State the blood parasite species.
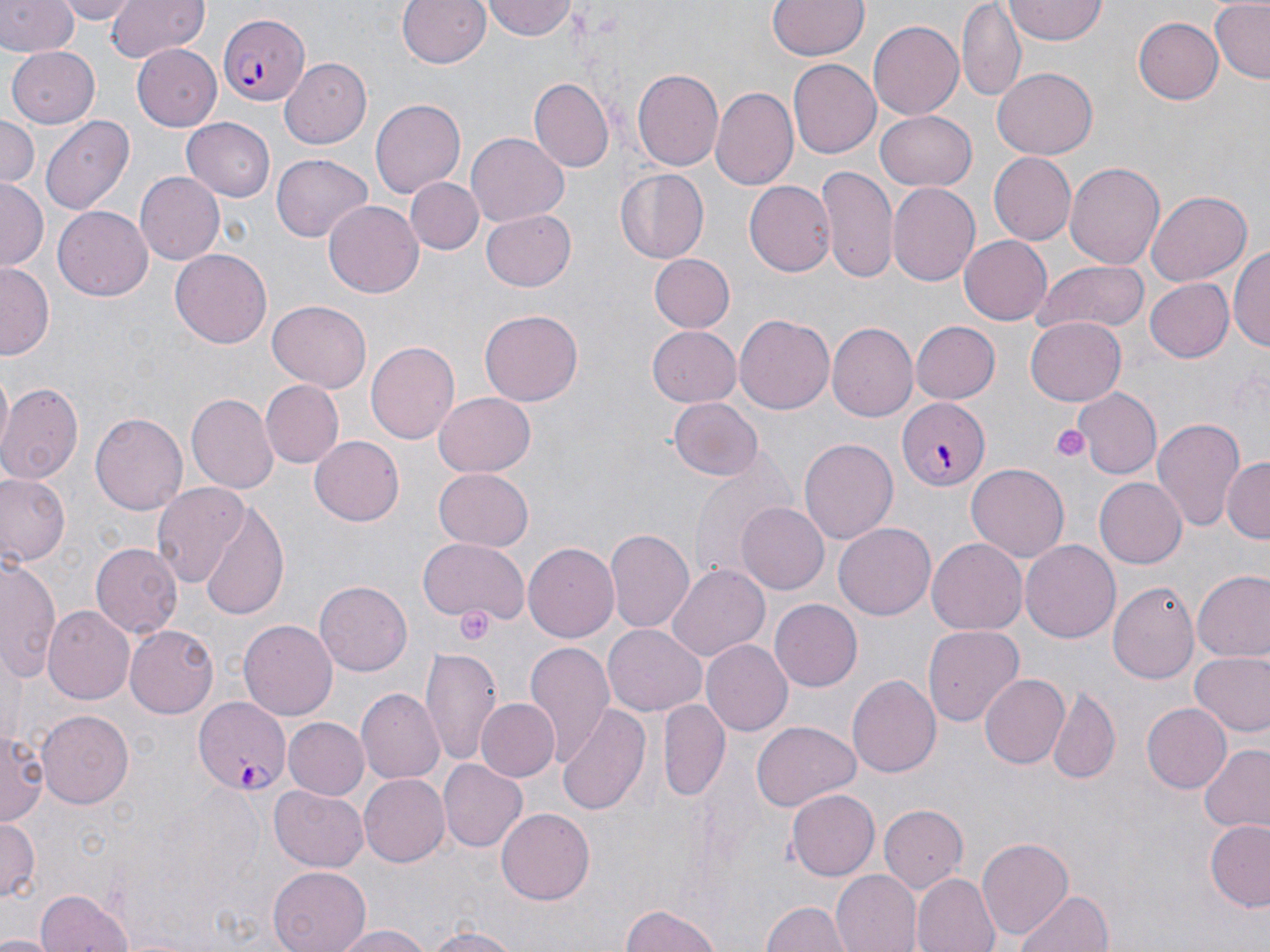
Plasmodium falciparum.

uninfected red blood cell locations = approximate bounding boxes as [x1, y1, x2, y2] in pixels: [0, 0, 76, 57], [56, 0, 140, 24], [103, 0, 209, 65], [396, 0, 492, 70], [481, 0, 578, 41], [767, 0, 868, 60], [1210, 0, 1269, 84], [957, 3, 1026, 101], [1005, 3, 1111, 44], [1134, 17, 1223, 105], [868, 21, 964, 121], [136, 44, 222, 133], [6, 47, 100, 127], [280, 58, 371, 148], [787, 59, 881, 158], [994, 69, 1097, 157], [632, 70, 722, 172], [531, 78, 614, 170], [710, 86, 798, 192], [371, 98, 464, 200], [876, 109, 977, 190], [0, 114, 38, 191], [182, 116, 276, 200], [42, 117, 135, 215], [467, 134, 568, 227], [991, 151, 1078, 245], [272, 155, 372, 244], [1065, 161, 1164, 270], [818, 166, 897, 282], [614, 169, 710, 264], [135, 172, 225, 266], [407, 178, 483, 253], [0, 179, 47, 268], [743, 180, 836, 276], [887, 182, 979, 287], [1147, 188, 1252, 284], [324, 200, 422, 298], [53, 204, 153, 297], [483, 209, 576, 291], [959, 234, 1052, 325], [1232, 242, 1270, 356], [170, 248, 273, 348], [647, 253, 735, 332], [1031, 261, 1150, 336], [0, 264, 52, 359], [1144, 278, 1234, 364], [266, 301, 371, 394], [480, 310, 582, 406], [734, 311, 834, 412], [1025, 319, 1125, 405], [910, 321, 1000, 404], [829, 322, 918, 422], [647, 326, 740, 406], [366, 340, 460, 443], [261, 380, 344, 467], [0, 382, 83, 487], [1073, 388, 1162, 480], [434, 391, 535, 476], [186, 393, 278, 494], [667, 397, 763, 481], [91, 412, 187, 515], [1153, 418, 1246, 533], [800, 435, 897, 541], [310, 436, 404, 526], [691, 452, 796, 578], [1220, 458, 1269, 544], [966, 462, 1070, 562], [433, 467, 534, 551], [0, 473, 70, 567], [1093, 478, 1186, 568], [151, 481, 251, 590], [736, 502, 830, 595], [199, 504, 289, 621], [834, 521, 934, 617], [606, 527, 695, 632], [927, 535, 1026, 632], [419, 538, 528, 626], [1021, 540, 1122, 643], [524, 541, 622, 642], [89, 543, 180, 639], [1, 557, 62, 684], [670, 564, 769, 661], [1192, 571, 1270, 664], [315, 579, 411, 676], [1108, 581, 1199, 683], [770, 599, 862, 692], [44, 606, 132, 704], [239, 619, 338, 720], [925, 624, 1023, 729], [603, 625, 707, 716], [126, 626, 217, 718], [703, 640, 793, 736], [526, 641, 616, 759], [421, 647, 501, 764], [1188, 652, 1269, 738], [848, 674, 941, 781], [978, 674, 1069, 770], [1049, 686, 1121, 785], [357, 688, 444, 785], [474, 698, 559, 781], [658, 699, 729, 801], [558, 703, 652, 813], [1140, 703, 1230, 792], [38, 710, 134, 810], [281, 718, 369, 800], [2, 722, 43, 829], [753, 722, 861, 810], [1198, 744, 1270, 835], [438, 759, 528, 852], [358, 774, 449, 868], [269, 785, 370, 872], [786, 788, 880, 881], [879, 804, 968, 894], [497, 808, 594, 905], [0, 817, 40, 903], [1205, 819, 1270, 912], [977, 837, 1073, 940], [268, 866, 370, 952], [831, 870, 922, 952], [912, 873, 1000, 952], [1011, 887, 1119, 952], [35, 888, 133, 952], [758, 901, 853, 952], [620, 902, 725, 952], [331, 922, 437, 951], [419, 926, 527, 952], [0, 934, 52, 952]
Plasmodium falciparum-infected red blood cell locations = approximate bounding boxes as [x1, y1, x2, y2] in pixels: [217, 13, 312, 107], [900, 398, 991, 490], [192, 700, 288, 795]
image size = 1270×952 pixels
magnification = 1000x
platelet locations = approximate bounding boxes as [x1, y1, x2, y2] in pixels: [1050, 425, 1090, 463], [455, 605, 498, 645]
modality = optical microscopy
preparation = thin blood film
stain = May-Grünwald-Giemsa
field of view = one of a larger specimen